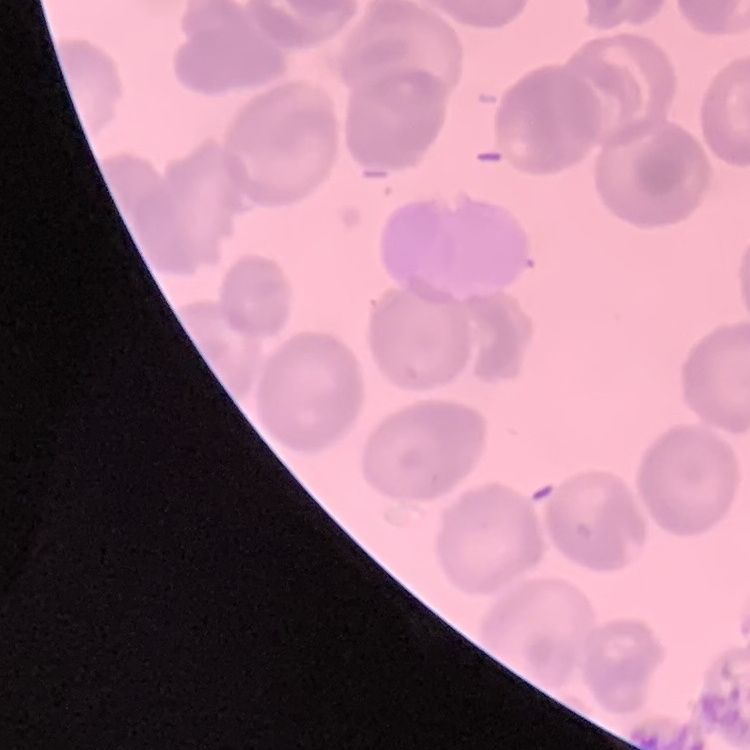
The red blood cells show no rouleaux formation. Field's or Giemsa stain. Thin peripheral smear. One tile cut from a larger photomicrograph.